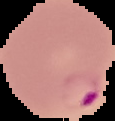
From a thin blood film. Image is 115×121 pixels. Segmented cell region on a black background. Malaria status: parasitized.